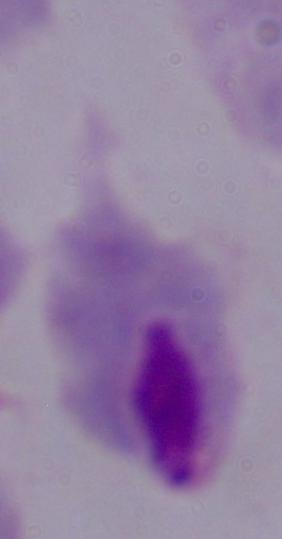
magnification = 1000x
identification = trichomonad
modality = photomicrograph